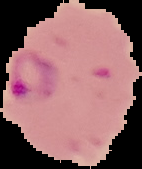

{
  "image_type": "segmented cell region with the area outside set to black",
  "result": "malaria parasites detected",
  "image_size": "142×169 pixels",
  "preparation": "thin blood smear"
}